Locate and identify every blood parasite.
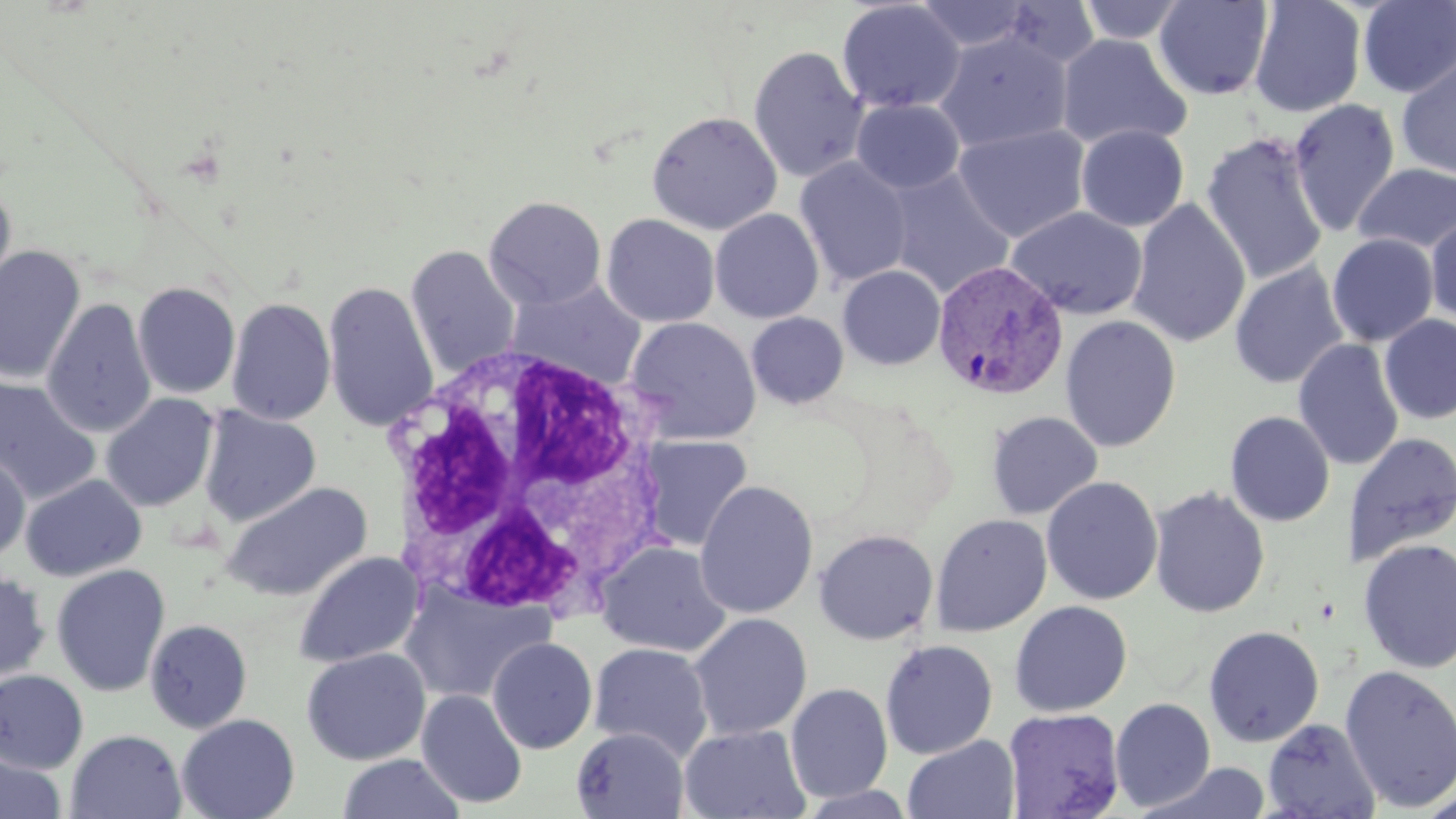
Approximate bounding boxes as named x1/y1/x2/y2 corners in pixels.
Plasmodium vivax-infected red blood cells: (x1=931, y1=259, x2=1069, y2=401).
No Plasmodium falciparum, Plasmodium ovale, Plasmodium malariae, Babesia divergens, or Trypanosoma brucei observed.

Summary:
  - Uninfected red blood cell locations: (x1=913, y1=0, x2=1035, y2=53), (x1=836, y1=1, x2=965, y2=114), (x1=1076, y1=1, x2=1189, y2=44), (x1=1154, y1=1, x2=1273, y2=101), (x1=1249, y1=1, x2=1366, y2=118), (x1=1358, y1=1, x2=1456, y2=98), (x1=934, y1=31, x2=1073, y2=153), (x1=1056, y1=33, x2=1192, y2=152), (x1=748, y1=45, x2=869, y2=183), (x1=1396, y1=55, x2=1456, y2=180), (x1=852, y1=98, x2=965, y2=194), (x1=1289, y1=98, x2=1400, y2=238), (x1=646, y1=111, x2=782, y2=235), (x1=953, y1=124, x2=1091, y2=243), (x1=1076, y1=125, x2=1189, y2=232), (x1=1201, y1=132, x2=1329, y2=286), (x1=795, y1=157, x2=913, y2=288), (x1=1353, y1=163, x2=1456, y2=254), (x1=884, y1=167, x2=1015, y2=299), (x1=0, y1=181, x2=17, y2=303), (x1=484, y1=196, x2=607, y2=309), (x1=1127, y1=198, x2=1250, y2=348), (x1=1006, y1=206, x2=1147, y2=320), (x1=710, y1=208, x2=824, y2=324), (x1=601, y1=213, x2=720, y2=327), (x1=1425, y1=214, x2=1456, y2=325), (x1=1327, y1=234, x2=1438, y2=346), (x1=0, y1=245, x2=86, y2=385), (x1=405, y1=245, x2=521, y2=381), (x1=1230, y1=262, x2=1348, y2=389), (x1=837, y1=265, x2=946, y2=370), (x1=506, y1=279, x2=647, y2=390), (x1=132, y1=281, x2=240, y2=399), (x1=322, y1=281, x2=439, y2=432), (x1=42, y1=297, x2=157, y2=438), (x1=226, y1=297, x2=336, y2=426), (x1=747, y1=312, x2=848, y2=409), (x1=1060, y1=315, x2=1181, y2=453), (x1=1378, y1=315, x2=1456, y2=425), (x1=624, y1=316, x2=761, y2=444), (x1=1293, y1=339, x2=1404, y2=471), (x1=0, y1=374, x2=101, y2=505), (x1=101, y1=393, x2=219, y2=512), (x1=199, y1=406, x2=321, y2=528), (x1=986, y1=410, x2=1102, y2=520), (x1=1224, y1=410, x2=1335, y2=527), (x1=1342, y1=432, x2=1456, y2=567), (x1=636, y1=435, x2=753, y2=552), (x1=0, y1=448, x2=30, y2=563), (x1=20, y1=474, x2=147, y2=582), (x1=1042, y1=476, x2=1163, y2=605), (x1=695, y1=480, x2=818, y2=619), (x1=222, y1=482, x2=372, y2=602), (x1=1149, y1=486, x2=1270, y2=618), (x1=930, y1=513, x2=1053, y2=637), (x1=813, y1=529, x2=938, y2=645), (x1=1357, y1=539, x2=1456, y2=674), (x1=597, y1=541, x2=732, y2=657), (x1=293, y1=551, x2=423, y2=668), (x1=51, y1=564, x2=171, y2=697), (x1=0, y1=569, x2=51, y2=685), (x1=400, y1=582, x2=553, y2=704), (x1=1009, y1=601, x2=1132, y2=717), (x1=688, y1=613, x2=812, y2=740), (x1=145, y1=619, x2=252, y2=733), (x1=1203, y1=625, x2=1325, y2=747), (x1=487, y1=637, x2=598, y2=754), (x1=880, y1=639, x2=998, y2=760), (x1=588, y1=643, x2=713, y2=763), (x1=301, y1=648, x2=430, y2=765), (x1=1339, y1=665, x2=1456, y2=812), (x1=0, y1=670, x2=88, y2=774), (x1=785, y1=682, x2=893, y2=803), (x1=416, y1=689, x2=527, y2=809), (x1=1110, y1=697, x2=1215, y2=811), (x1=1003, y1=708, x2=1125, y2=819), (x1=177, y1=713, x2=300, y2=819), (x1=1263, y1=717, x2=1381, y2=819), (x1=679, y1=724, x2=811, y2=819), (x1=571, y1=727, x2=689, y2=818), (x1=66, y1=729, x2=187, y2=819), (x1=903, y1=735, x2=1020, y2=819), (x1=338, y1=753, x2=465, y2=818), (x1=0, y1=755, x2=66, y2=819), (x1=1148, y1=761, x2=1273, y2=818)
  - White blood cell locations: (x1=374, y1=343, x2=671, y2=628)
  - Slide-level diagnosis: Plasmodium vivax
  - Image size: 1456×819 pixels
  - Stain: May-Grünwald-Giemsa
  - Magnification: 1000x
  - Modality: optical microscopy
  - Field of view: single
  - Preparation: thin blood smear